Identify the blood parasite species.
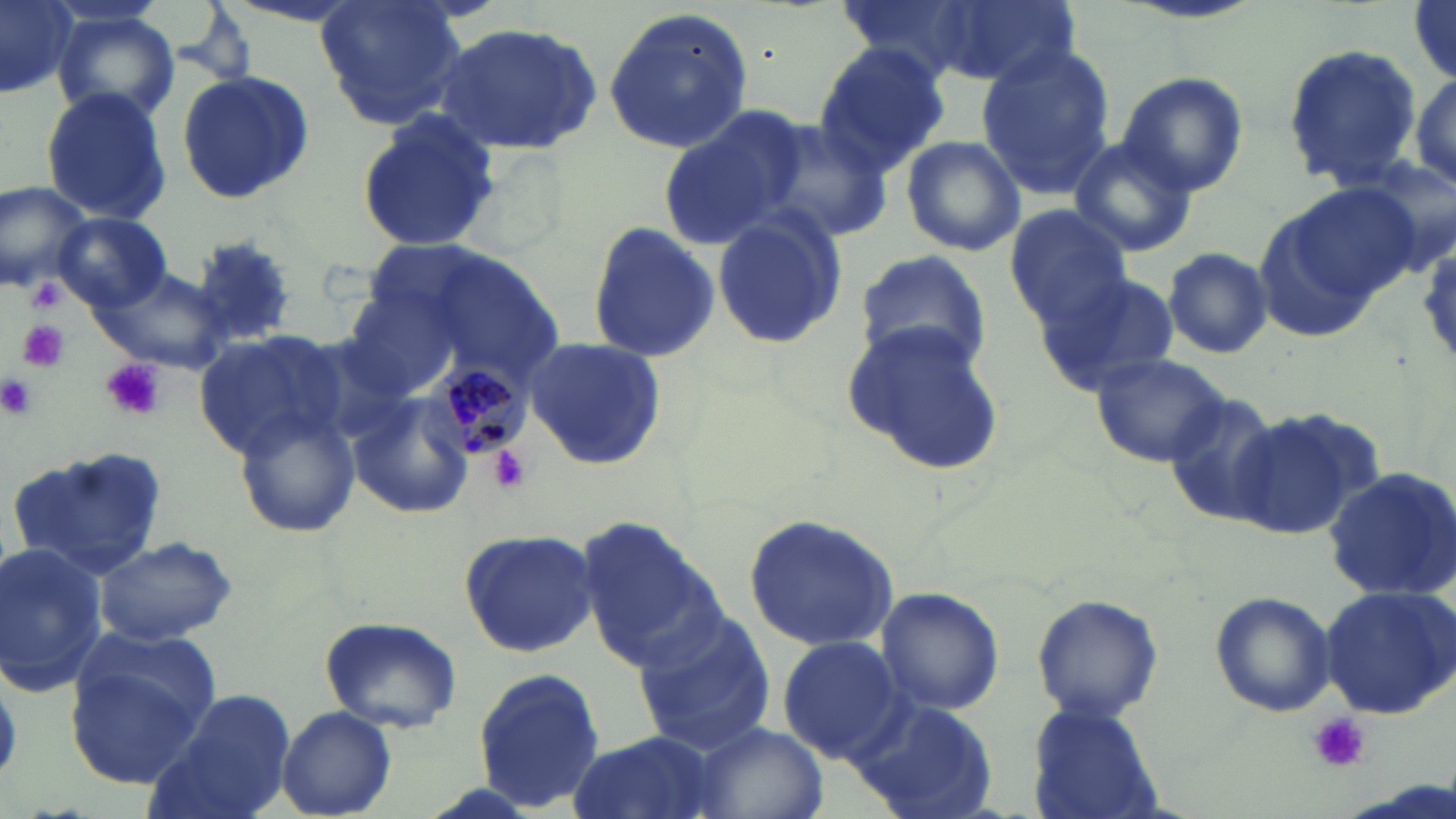

Plasmodium malariae.

Approximate bounding boxes as (x1,y1)-(x2,y2) corner pairs in pixels. Uninfected red blood cell locations: (0,0)-(79,101), (315,0)-(467,128), (930,0)-(1084,88), (1409,1)-(1456,84), (603,7)-(753,154), (53,10)-(183,129), (436,20)-(606,156), (1281,42)-(1423,188), (812,43)-(951,175), (977,46)-(1115,199), (1408,62)-(1456,204), (173,67)-(316,204), (1118,72)-(1248,196), (40,88)-(173,222), (658,106)-(812,250), (354,107)-(504,254), (752,113)-(889,241), (899,134)-(1026,256), (1066,135)-(1199,260), (0,178)-(92,295), (1284,182)-(1427,307), (1248,200)-(1387,341), (1003,205)-(1132,323), (710,209)-(846,353), (54,213)-(171,310), (585,221)-(721,364), (1163,248)-(1272,357), (853,249)-(992,375), (93,264)-(230,371), (1036,271)-(1178,394), (843,324)-(1005,473), (193,330)-(353,459), (521,337)-(667,471), (1087,352)-(1231,468), (1156,390)-(1287,527), (345,392)-(475,521), (1228,408)-(1371,541), (232,409)-(360,538), (7,444)-(167,575), (1320,469)-(1456,602), (577,512)-(724,672), (742,512)-(903,651), (457,528)-(599,656), (94,536)-(237,645), (0,542)-(110,696), (1319,584)-(1456,720), (876,586)-(1004,715), (1210,591)-(1336,717), (1030,594)-(1165,722), (630,607)-(776,756), (319,615)-(462,733), (76,627)-(222,735), (775,637)-(906,764), (67,662)-(209,788), (0,666)-(20,786), (472,668)-(606,809), (149,690)-(297,819), (843,693)-(1002,818), (1026,701)-(1166,819), (276,705)-(397,819), (685,720)-(829,819), (564,732)-(722,819). Plasmodium malariae-infected red blood cell locations: (423,358)-(533,461). Platelet locations: (27,279)-(65,313), (19,319)-(69,373), (100,357)-(166,422), (0,373)-(37,421), (490,445)-(531,493), (1309,712)-(1368,773). May-Grünwald-Giemsa-stained preparation. 1000x magnification. Image is 1456×819 pixels. One field of a larger specimen. Thin blood smear. Optical microscopy.